State which parasite is depicted.
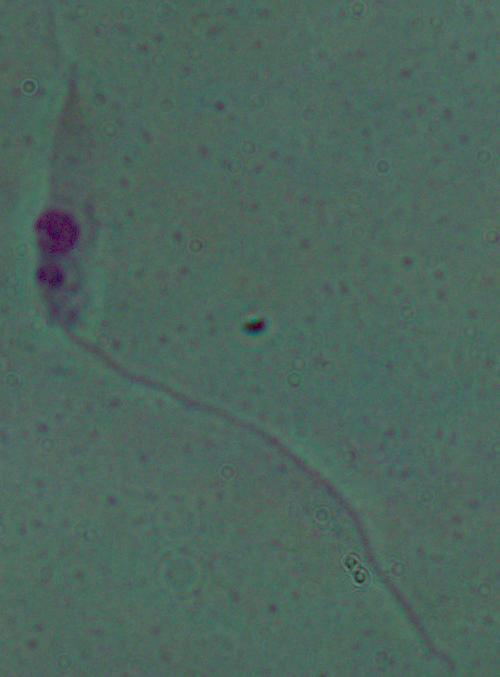

This is Leishmania.

Summary:
  - Modality: micrograph
  - Magnification: 1000x